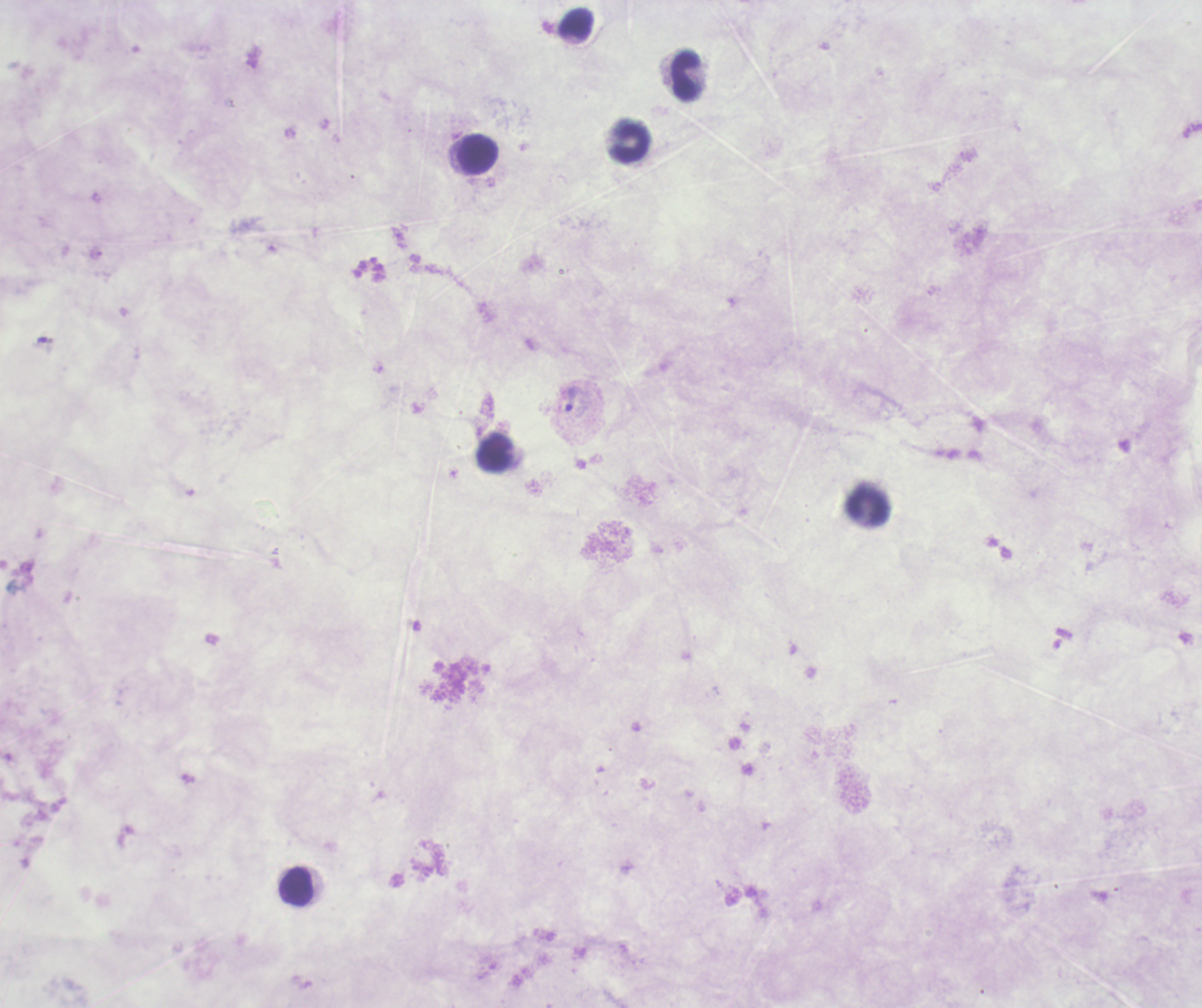
coordinate format = approximate centers as {x, y} in pixels
trophozoite locations = {42, 339}, {571, 399}
leukocyte locations = {575, 25}, {686, 75}, {629, 141}, {477, 154}, {495, 452}, {869, 508}, {297, 886}
field of view = single
magnification = 100x
background quality = unsatisfactory
stain = Romanowsky
coloration quality = bad
result = positive for malaria parasites
context = previously used in a real diagnosis
image size = 1202×1008 pixels
preparation = thick blood film